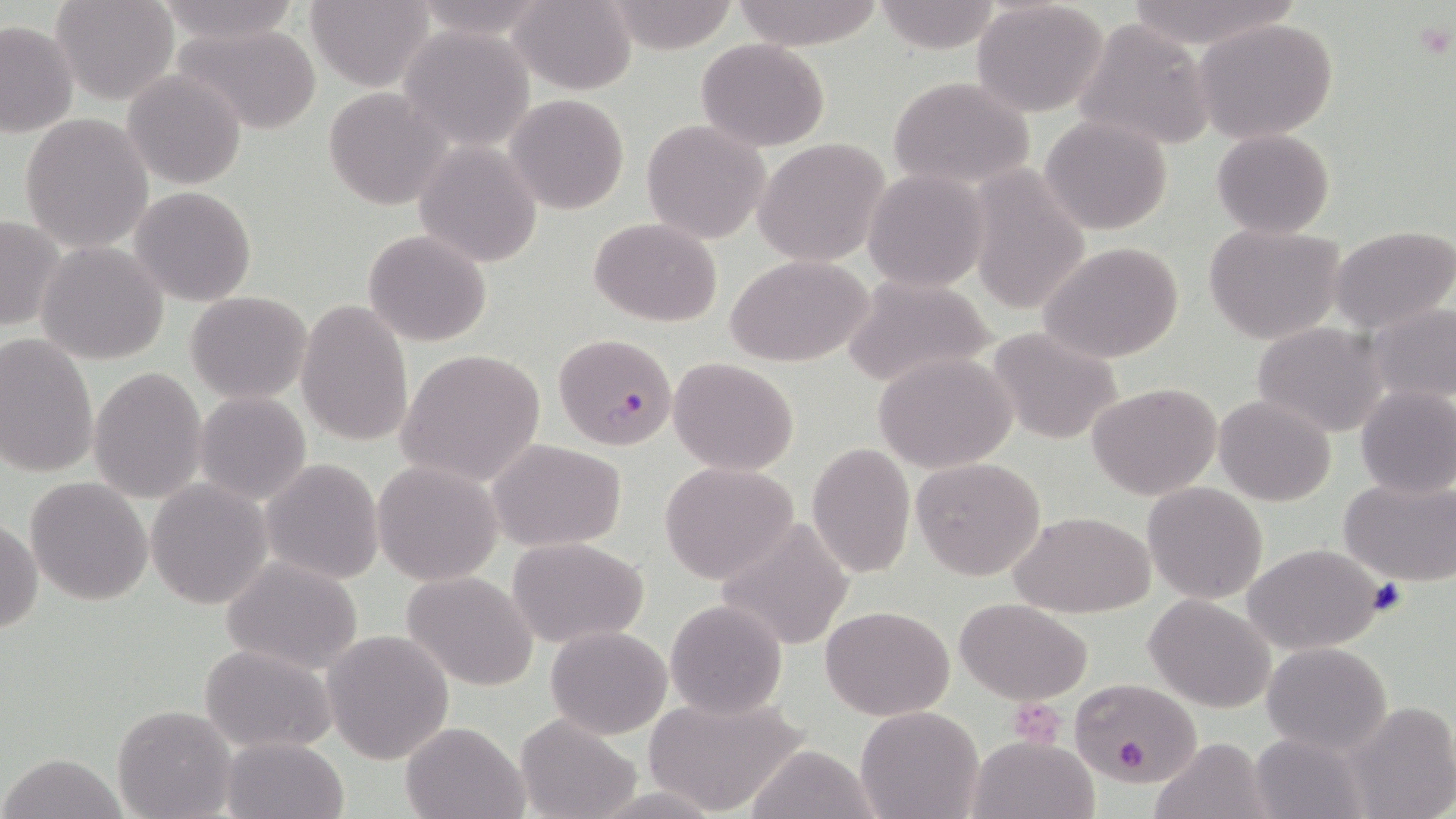
Approximate bounding boxes as [x1, y1, x2, y2] in pixels. Uninfected red blood cell locations: [52, 0, 180, 105], [152, 0, 302, 45], [305, 0, 437, 91], [509, 0, 637, 95], [732, 0, 889, 49], [870, 0, 1005, 52], [1120, 0, 1299, 49], [600, 1, 742, 53], [971, 1, 1112, 118], [1194, 17, 1339, 145], [1072, 18, 1214, 152], [0, 20, 79, 138], [171, 22, 324, 134], [398, 26, 534, 150], [695, 39, 831, 152], [122, 68, 248, 191], [352, 68, 513, 196], [888, 76, 1035, 191], [323, 88, 450, 209], [504, 93, 629, 214], [19, 112, 153, 253], [1038, 113, 1174, 237], [642, 120, 771, 245], [1211, 129, 1334, 239], [754, 137, 893, 268], [414, 141, 543, 267], [964, 162, 1092, 314], [864, 169, 989, 292], [128, 186, 257, 308], [991, 193, 1143, 342], [0, 214, 65, 332], [589, 218, 725, 327], [1201, 222, 1347, 344], [1330, 225, 1455, 335], [363, 229, 492, 347], [36, 240, 169, 366], [1038, 242, 1185, 363], [726, 254, 875, 369], [840, 273, 997, 389], [185, 290, 312, 403], [297, 299, 415, 446], [1367, 302, 1456, 409], [1253, 322, 1390, 437], [986, 326, 1123, 446], [0, 333, 99, 478], [395, 348, 547, 488], [873, 352, 1018, 474], [668, 356, 800, 476], [89, 367, 208, 505], [1088, 382, 1221, 499], [1355, 385, 1456, 499], [193, 391, 312, 503], [1213, 395, 1338, 506], [488, 439, 625, 551], [807, 441, 916, 578], [910, 457, 1046, 581], [261, 459, 383, 584], [373, 460, 505, 587], [659, 461, 802, 586], [25, 476, 153, 605], [1339, 476, 1456, 586], [145, 479, 272, 609], [1143, 481, 1269, 604], [1012, 510, 1155, 617], [715, 515, 858, 652], [1, 518, 42, 634], [506, 536, 650, 648], [1241, 542, 1388, 655], [221, 555, 366, 675], [401, 571, 539, 691], [1144, 594, 1276, 712], [957, 597, 1093, 704], [664, 599, 787, 720], [820, 604, 955, 720], [545, 624, 672, 738], [322, 628, 454, 765], [1262, 641, 1393, 755], [198, 644, 338, 753], [1071, 676, 1202, 786], [641, 692, 812, 816], [1346, 701, 1456, 819], [855, 704, 984, 819], [111, 705, 236, 818], [514, 713, 641, 819], [400, 720, 531, 818], [1248, 731, 1367, 819], [970, 735, 1097, 818], [1152, 736, 1269, 819], [220, 737, 348, 818], [745, 744, 881, 819], [2, 752, 126, 818]. Platelet locations: [1412, 21, 1454, 60], [1367, 579, 1408, 618], [1009, 699, 1067, 744], [1113, 738, 1150, 776]. Plasmodium falciparum-infected red blood cell locations: [553, 333, 679, 450]. Slide-level diagnosis: Plasmodium falciparum. Image is 1456×819 pixels. One field of a larger specimen. May-Grünwald-Giemsa-stained preparation. Light microscopy. Thin blood film. Captured at 1000x magnification.